Assess this cell for malaria.
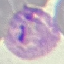

It is parasitized.

Thin smear of blood. Cell patch, automatically extracted from a larger field of view and resized to 64 × 64 pixels. Giemsa-stained preparation. Photographed with a smartphone camera at the microscope eyepiece.